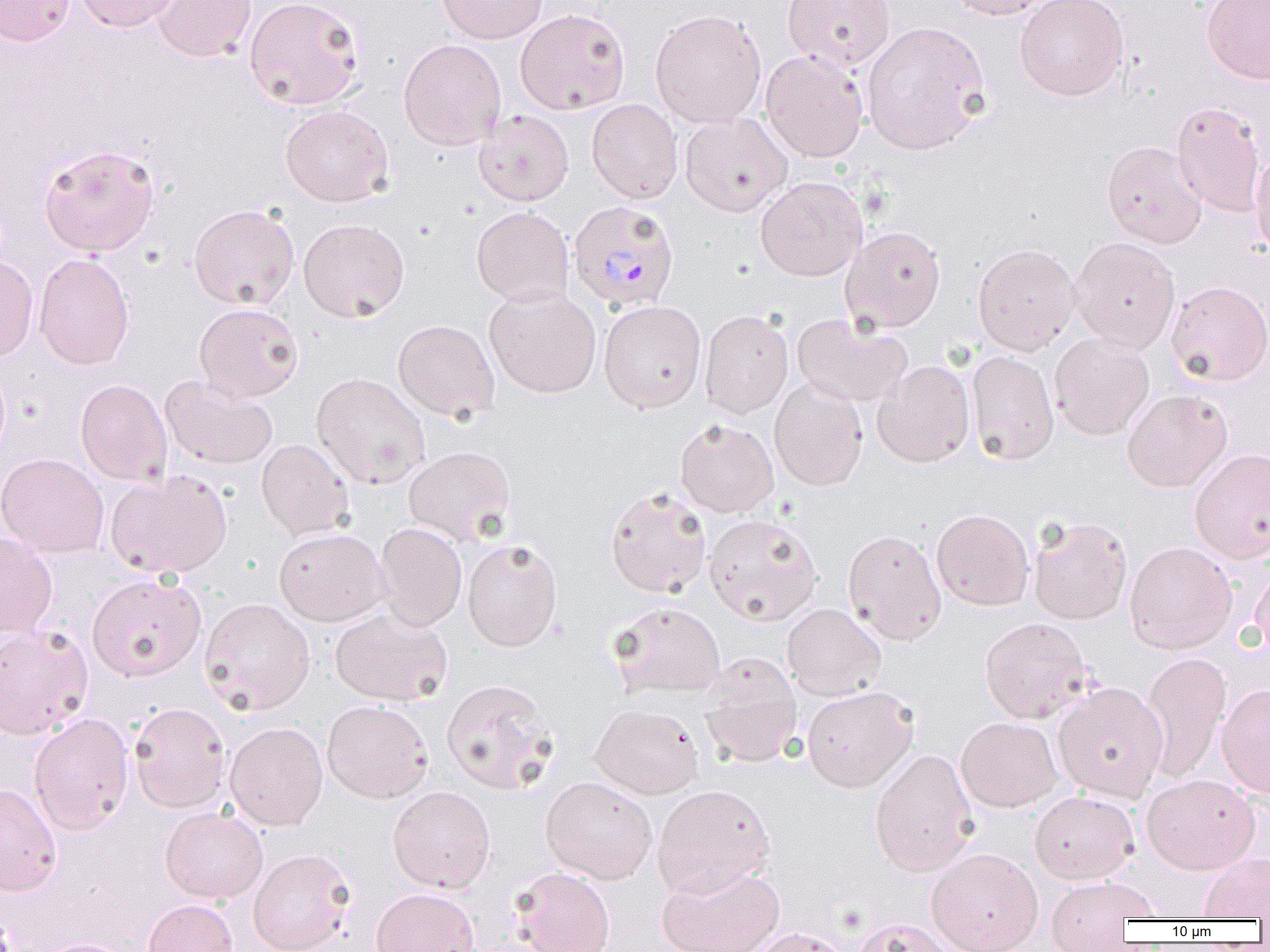
Plasmodium malariae-infected red blood cell locations = approximate bounding boxes as named x1/y1/x2/y2 corners in pixels: (x1=568, y1=200, x2=680, y2=312)
slide-level diagnosis = Plasmodium malariae
modality = optical microscopy
magnification = 1000x
preparation = thin blood smear
uninfected red blood cell locations = approximate bounding boxes as named x1/y1/x2/y2 corners in pixels: (x1=0, y1=0, x2=76, y2=46), (x1=76, y1=0, x2=181, y2=33), (x1=151, y1=0, x2=257, y2=63), (x1=243, y1=0, x2=365, y2=111), (x1=436, y1=0, x2=548, y2=45), (x1=782, y1=0, x2=895, y2=72), (x1=943, y1=0, x2=1061, y2=20), (x1=1014, y1=0, x2=1130, y2=101), (x1=1201, y1=0, x2=1270, y2=85), (x1=514, y1=8, x2=631, y2=116), (x1=649, y1=9, x2=767, y2=129), (x1=861, y1=21, x2=991, y2=155), (x1=398, y1=39, x2=507, y2=150), (x1=759, y1=50, x2=868, y2=163), (x1=587, y1=99, x2=684, y2=204), (x1=1170, y1=101, x2=1267, y2=219), (x1=279, y1=105, x2=393, y2=207), (x1=473, y1=110, x2=574, y2=207), (x1=679, y1=113, x2=792, y2=216), (x1=1102, y1=141, x2=1208, y2=248), (x1=38, y1=144, x2=160, y2=257), (x1=1251, y1=148, x2=1270, y2=258), (x1=755, y1=176, x2=867, y2=282), (x1=188, y1=203, x2=299, y2=311), (x1=471, y1=206, x2=574, y2=307), (x1=298, y1=218, x2=410, y2=323), (x1=840, y1=225, x2=946, y2=334), (x1=1069, y1=237, x2=1181, y2=353), (x1=972, y1=243, x2=1079, y2=356), (x1=34, y1=253, x2=135, y2=371), (x1=0, y1=256, x2=39, y2=361), (x1=1166, y1=280, x2=1270, y2=387), (x1=484, y1=287, x2=602, y2=399), (x1=598, y1=300, x2=707, y2=413), (x1=194, y1=303, x2=304, y2=402), (x1=699, y1=309, x2=794, y2=420), (x1=792, y1=312, x2=913, y2=409), (x1=392, y1=319, x2=499, y2=423), (x1=1049, y1=332, x2=1155, y2=441), (x1=966, y1=350, x2=1059, y2=466), (x1=872, y1=360, x2=975, y2=468), (x1=311, y1=372, x2=431, y2=490), (x1=160, y1=374, x2=278, y2=471), (x1=75, y1=379, x2=173, y2=486), (x1=769, y1=379, x2=868, y2=492), (x1=1121, y1=389, x2=1233, y2=493), (x1=675, y1=419, x2=779, y2=517), (x1=256, y1=438, x2=355, y2=541), (x1=404, y1=446, x2=516, y2=548), (x1=1189, y1=449, x2=1270, y2=565), (x1=0, y1=453, x2=109, y2=558), (x1=105, y1=469, x2=232, y2=579), (x1=605, y1=486, x2=712, y2=597), (x1=931, y1=508, x2=1034, y2=611), (x1=703, y1=513, x2=823, y2=626), (x1=1027, y1=515, x2=1133, y2=625), (x1=373, y1=522, x2=467, y2=632), (x1=273, y1=528, x2=390, y2=626), (x1=842, y1=529, x2=947, y2=646), (x1=0, y1=532, x2=58, y2=638), (x1=462, y1=538, x2=563, y2=652), (x1=1124, y1=541, x2=1238, y2=655), (x1=1250, y1=560, x2=1270, y2=660), (x1=86, y1=573, x2=206, y2=681), (x1=198, y1=597, x2=315, y2=715), (x1=608, y1=602, x2=726, y2=700), (x1=782, y1=603, x2=886, y2=702), (x1=330, y1=607, x2=452, y2=706), (x1=979, y1=617, x2=1093, y2=724), (x1=0, y1=624, x2=93, y2=740), (x1=1139, y1=651, x2=1231, y2=784), (x1=698, y1=653, x2=802, y2=769), (x1=441, y1=678, x2=560, y2=795), (x1=1052, y1=681, x2=1169, y2=802), (x1=1216, y1=683, x2=1270, y2=799), (x1=801, y1=685, x2=918, y2=792), (x1=322, y1=700, x2=433, y2=803), (x1=128, y1=702, x2=231, y2=813), (x1=590, y1=703, x2=704, y2=799), (x1=28, y1=712, x2=135, y2=835), (x1=955, y1=717, x2=1063, y2=813), (x1=225, y1=722, x2=328, y2=831), (x1=869, y1=748, x2=979, y2=878), (x1=1141, y1=773, x2=1260, y2=874), (x1=540, y1=775, x2=658, y2=884), (x1=0, y1=782, x2=62, y2=896), (x1=652, y1=784, x2=776, y2=899), (x1=388, y1=786, x2=495, y2=892), (x1=1029, y1=790, x2=1139, y2=884), (x1=159, y1=805, x2=268, y2=904), (x1=926, y1=847, x2=1043, y2=952), (x1=248, y1=848, x2=355, y2=952), (x1=1199, y1=852, x2=1270, y2=919), (x1=656, y1=863, x2=786, y2=952), (x1=511, y1=866, x2=615, y2=952), (x1=1044, y1=875, x2=1161, y2=936), (x1=371, y1=887, x2=479, y2=952), (x1=143, y1=899, x2=239, y2=952), (x1=852, y1=918, x2=958, y2=952), (x1=743, y1=927, x2=856, y2=952), (x1=34, y1=938, x2=138, y2=952)
field of view = one of a larger specimen
image size = 1270×952 pixels